Give the preparation type.
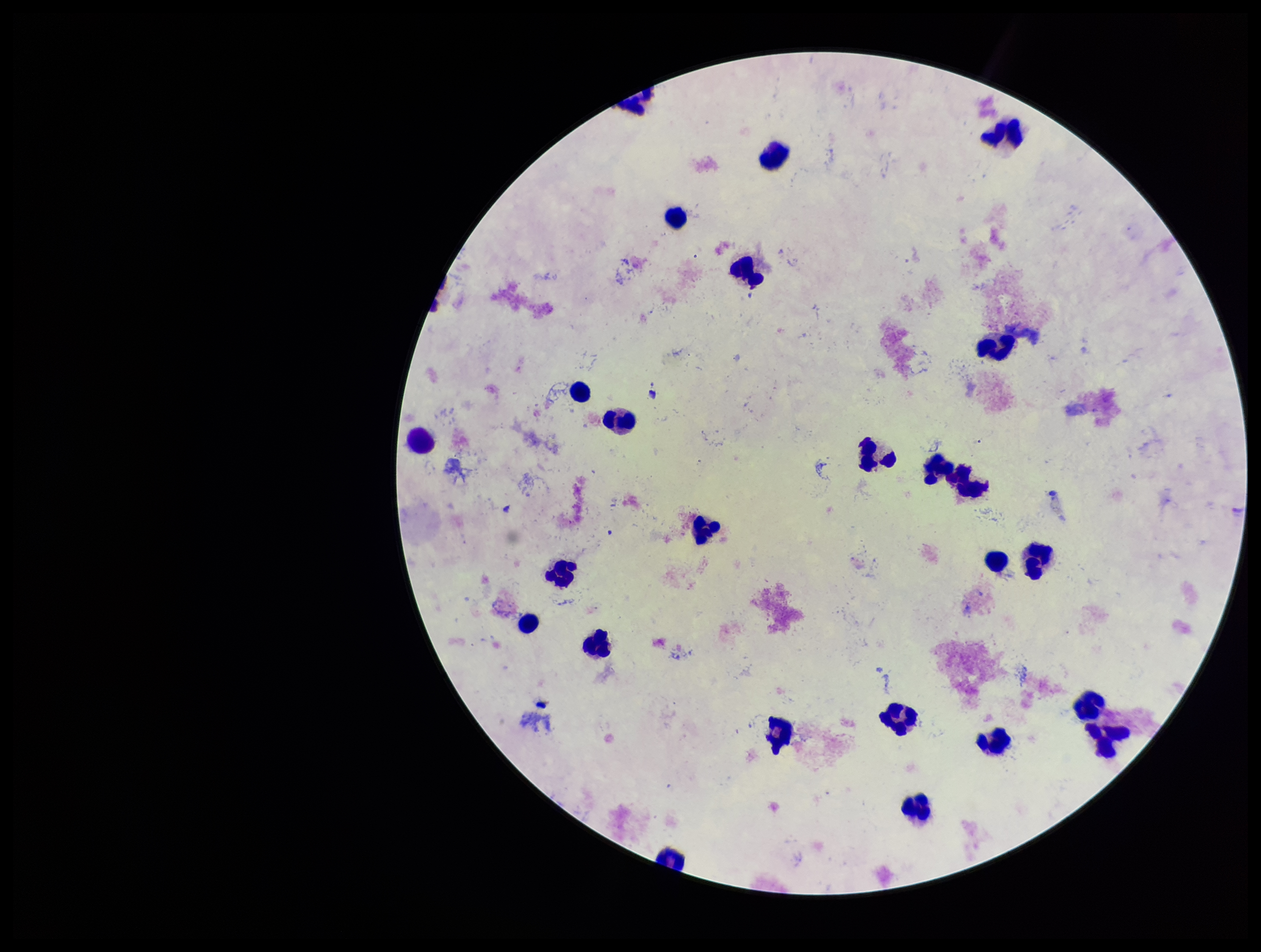

A thick smear.

Patient malaria status: positive. Plasmodium parasites: none identified. Image is 1261×952 pixels. Single field of view. Species reported for this patient: Plasmodium vivax. Leukocyte count: 24. Giemsa stain. Parasite count: 0. Photographed through the microscope eyepiece with a smartphone camera.